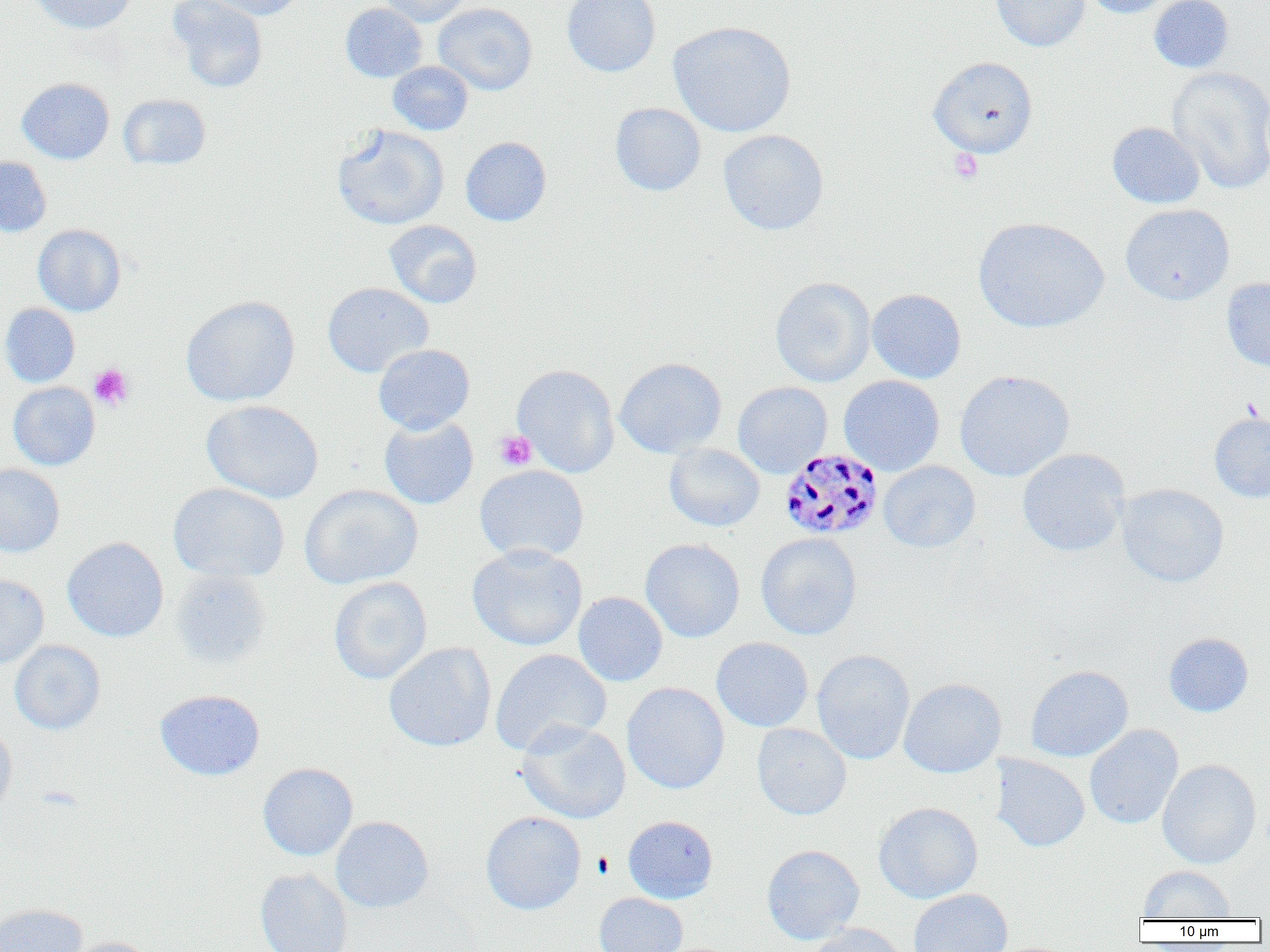
Summary:
  - Coordinate format: approximate bounding boxes as (x1, y1, x2, y2) in pixels
  - Plasmodium malariae-infected red blood cell locations: (778, 448, 882, 541)
  - Uninfected red blood cell locations: (30, 0, 138, 34), (167, 0, 268, 93), (200, 0, 303, 21), (379, 0, 472, 26), (561, 0, 661, 77), (990, 0, 1089, 51), (1080, 0, 1174, 18), (1149, 0, 1234, 73), (340, 2, 428, 82), (433, 2, 537, 95), (668, 20, 797, 137), (928, 56, 1038, 158), (387, 61, 473, 135), (1167, 65, 1270, 194), (17, 77, 114, 164), (118, 94, 210, 170), (610, 103, 706, 196), (1107, 121, 1205, 208), (332, 124, 449, 230), (718, 130, 829, 235), (460, 136, 552, 226), (0, 155, 52, 237), (1120, 203, 1234, 305), (973, 217, 1109, 333), (384, 219, 482, 308), (32, 224, 126, 316), (770, 276, 876, 387), (1221, 277, 1270, 372), (322, 282, 433, 377), (867, 289, 966, 383), (180, 295, 300, 406), (0, 303, 80, 387), (373, 344, 475, 434), (614, 357, 727, 458), (512, 364, 620, 477), (954, 369, 1074, 482), (838, 375, 945, 475), (733, 381, 832, 477), (8, 382, 100, 470), (201, 399, 323, 503), (1209, 413, 1270, 502), (379, 415, 478, 509), (664, 443, 764, 531), (1017, 448, 1129, 556), (879, 461, 980, 552), (0, 464, 65, 557), (474, 464, 589, 563), (168, 482, 289, 582), (1116, 483, 1229, 587), (299, 485, 423, 589), (756, 533, 862, 640), (62, 537, 169, 642), (640, 538, 745, 642), (467, 543, 588, 651), (171, 568, 271, 668), (0, 574, 49, 669), (329, 576, 432, 684), (573, 591, 668, 687), (1164, 632, 1253, 717), (711, 637, 813, 732), (10, 640, 106, 735), (384, 642, 496, 752), (490, 648, 611, 756), (812, 649, 915, 764), (1025, 665, 1133, 762), (898, 678, 1007, 778), (622, 682, 729, 793), (155, 689, 265, 780), (516, 720, 631, 823), (0, 722, 17, 819), (752, 722, 851, 820), (1085, 724, 1183, 829), (991, 754, 1089, 852), (1157, 759, 1261, 869), (258, 763, 358, 860), (873, 802, 983, 903), (480, 811, 586, 915), (623, 815, 718, 903), (331, 816, 434, 912), (762, 844, 864, 944), (1138, 866, 1236, 920), (255, 867, 354, 952), (909, 889, 1012, 952), (594, 892, 687, 952), (0, 903, 87, 952), (806, 923, 909, 952), (59, 936, 157, 952)
  - Platelet locations: (948, 148, 983, 183), (88, 363, 134, 410), (494, 430, 537, 471)
  - Slide-level diagnosis: Plasmodium malariae
  - Image size: 1270×952 pixels
  - Field of view: one of a larger specimen
  - Magnification: 1000x
  - Modality: light microscopy
  - Preparation: thin blood film